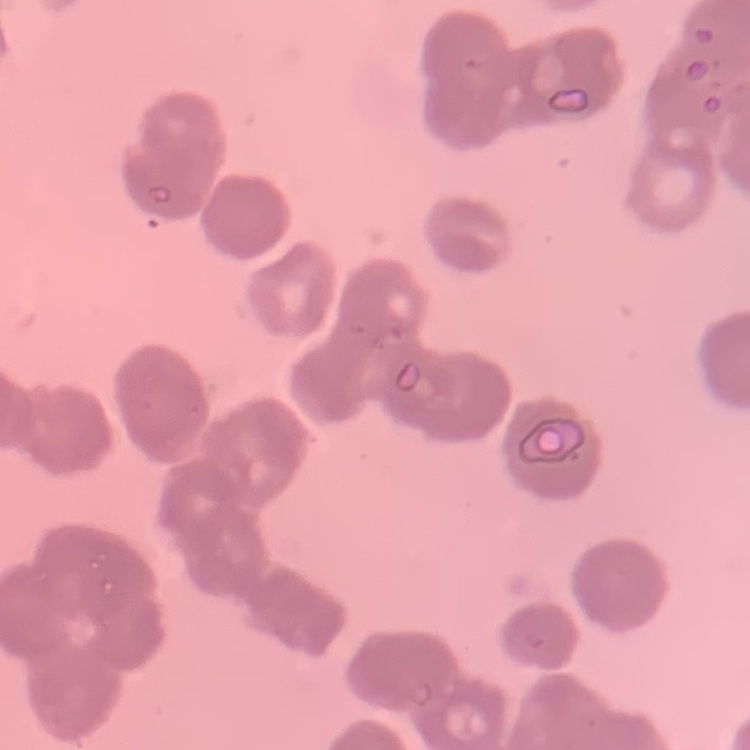
The red blood cells show rouleaux formation. Thin blood film. One tile cut from a larger photomicrograph. Field's or Giemsa stain.